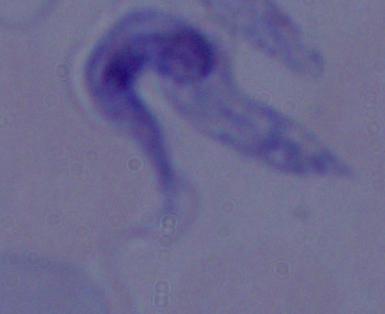

A trypanosome is seen. Photomicrograph. Captured at 1000x magnification.